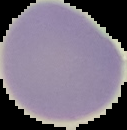

image_size: 127×130 pixels
preparation: thin blood smear
image_type: segmented cell region with the area outside set to black
malaria_status: uninfected